Describe the morphology of the red blood cells.
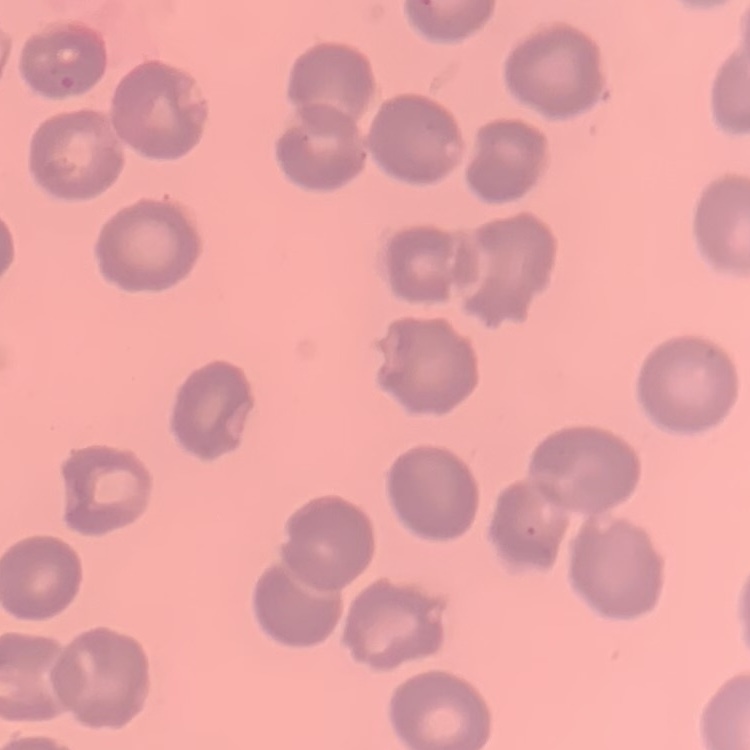
No rouleaux formation.

Summary:
  - Preparation: thin blood smear
  - Stain: Field's or Giemsa
  - Image type: one tile cut from a larger photomicrograph